Name the blood parasite species.
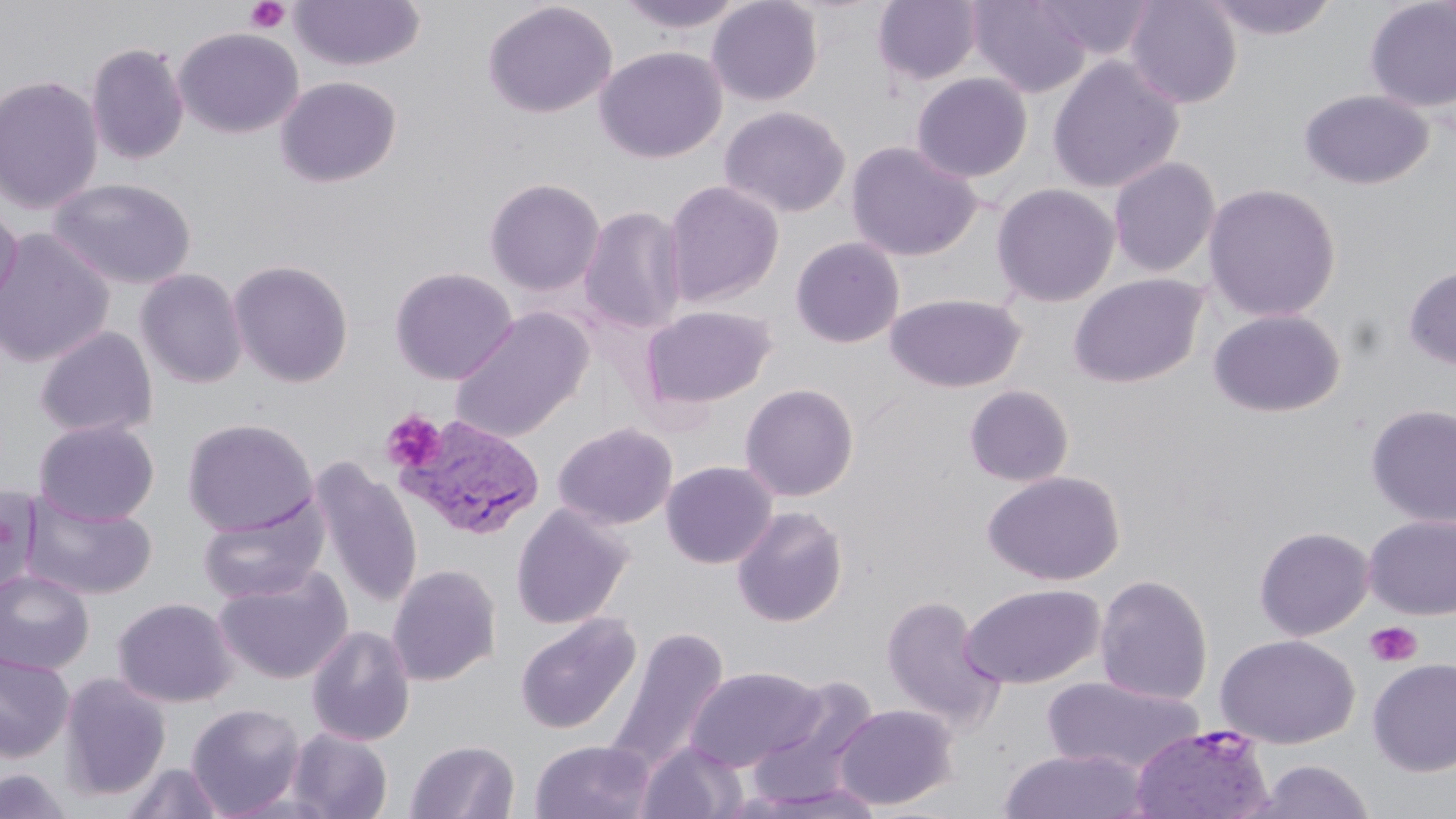
Plasmodium vivax.

Approximate bounding boxes as [x1, y1, x2, y2] in pixels. Platelet locations: [244, 0, 291, 34], [381, 410, 447, 473], [1364, 621, 1423, 668]. Uninfected red blood cell locations: [289, 0, 425, 72], [615, 0, 747, 35], [706, 0, 824, 106], [873, 0, 982, 87], [966, 0, 1093, 97], [1030, 0, 1157, 62], [1124, 0, 1243, 108], [1201, 0, 1340, 41], [481, 1, 617, 119], [1365, 1, 1456, 113], [174, 27, 303, 138], [86, 42, 189, 165], [594, 46, 727, 163], [1047, 55, 1184, 193], [910, 72, 1034, 183], [0, 75, 104, 215], [275, 76, 403, 188], [1298, 89, 1434, 190], [718, 105, 851, 218], [845, 141, 983, 261], [1107, 156, 1221, 278], [47, 177, 196, 289], [484, 177, 606, 296], [661, 179, 785, 307], [990, 182, 1121, 307], [1202, 182, 1342, 323], [1, 204, 23, 319], [578, 205, 689, 334], [0, 228, 115, 367], [789, 236, 906, 348], [228, 259, 354, 387], [1403, 265, 1456, 371], [389, 266, 518, 385], [135, 269, 249, 389], [1068, 273, 1208, 388], [884, 293, 1026, 393], [640, 304, 778, 410], [449, 308, 594, 444], [1207, 308, 1346, 417], [34, 326, 158, 438], [739, 383, 859, 502], [963, 384, 1075, 488], [1365, 403, 1456, 527], [183, 418, 318, 536], [34, 420, 159, 525], [553, 422, 678, 530], [310, 459, 423, 608], [661, 460, 778, 569], [981, 469, 1125, 586], [0, 484, 42, 599], [20, 493, 157, 601], [198, 499, 328, 604], [511, 503, 634, 629], [732, 505, 848, 627], [1363, 514, 1456, 619], [1254, 525, 1375, 641], [387, 564, 502, 686], [214, 566, 354, 685], [0, 570, 95, 675], [1094, 573, 1214, 706], [960, 583, 1106, 689], [879, 595, 1003, 728], [112, 597, 238, 708], [513, 612, 642, 736], [306, 624, 416, 746], [604, 627, 730, 778], [1215, 634, 1359, 748], [0, 652, 74, 762], [1367, 658, 1456, 776], [685, 666, 828, 772], [57, 673, 171, 801], [748, 676, 881, 808], [1041, 676, 1204, 774], [186, 703, 306, 817], [832, 703, 958, 810], [286, 727, 393, 819], [405, 739, 519, 819], [529, 739, 656, 819], [635, 740, 749, 819], [998, 747, 1150, 819], [1251, 758, 1377, 818], [120, 761, 226, 818], [0, 768, 74, 818], [740, 784, 888, 818]. Plasmodium vivax-infected red blood cell locations: [398, 415, 546, 541], [1129, 724, 1275, 819]. One field of a larger specimen. Thin blood smear. Light microscopy. Captured at 1000x magnification. Image is 1456×819 pixels. May-Grünwald-Giemsa stain.